Identify the blood parasite species.
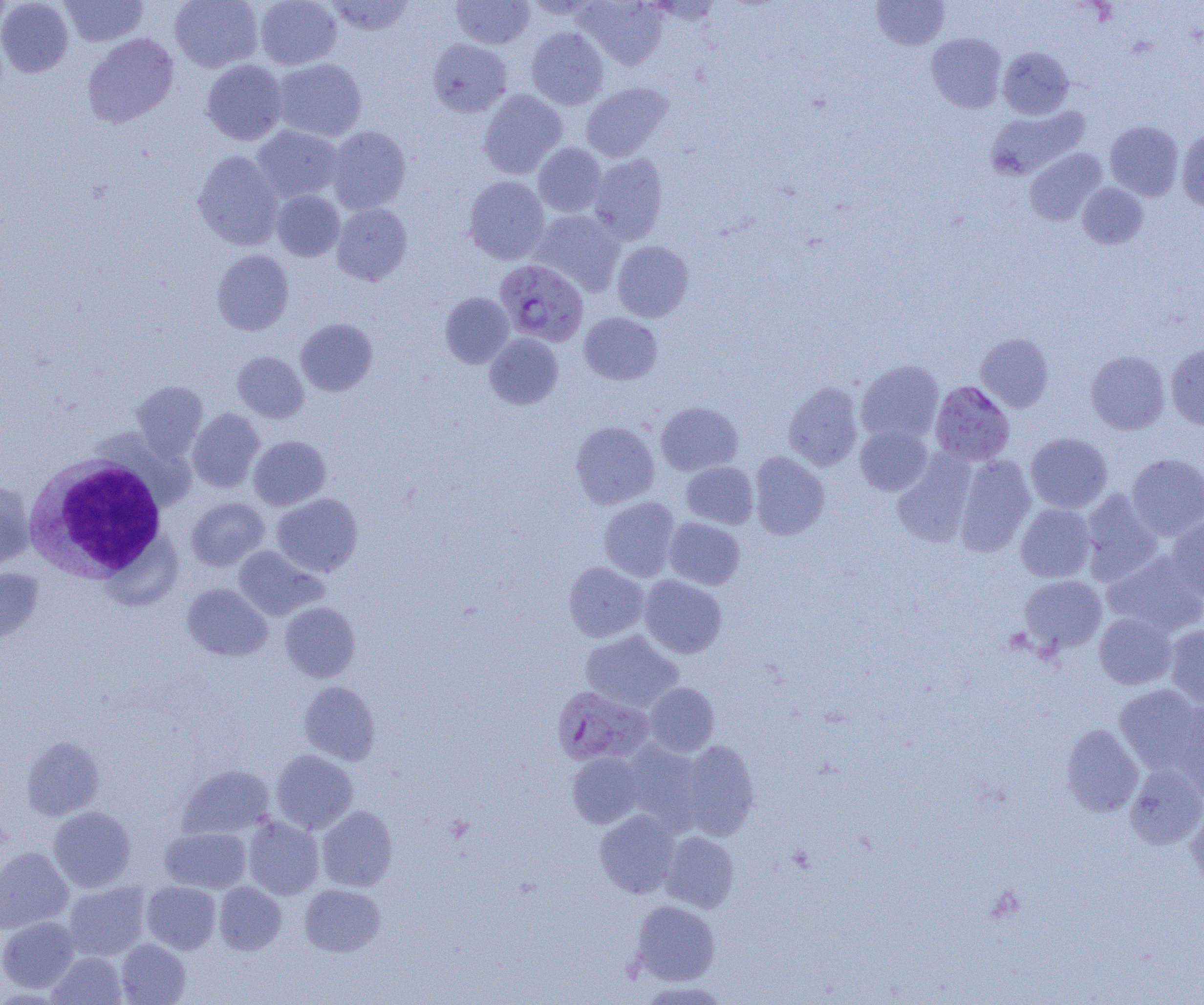
Plasmodium falciparum.

Summary:
  - Coordinate format: approximate bounding boxes as (x1, y1, x2, y2) in pixels
  - Uninfected red blood cell locations: (0, 0, 13, 32), (0, 0, 74, 77), (60, 0, 148, 46), (170, 0, 262, 72), (255, 0, 342, 70), (326, 0, 415, 37), (451, 0, 535, 49), (576, 0, 667, 70), (871, 0, 950, 50), (526, 27, 609, 109), (82, 33, 179, 128), (926, 33, 1007, 113), (427, 39, 512, 117), (998, 46, 1074, 119), (272, 58, 367, 141), (202, 60, 287, 145), (581, 82, 672, 162), (478, 89, 567, 178), (986, 105, 1089, 181), (1105, 121, 1184, 201), (252, 125, 342, 203), (326, 126, 411, 214), (1176, 129, 1204, 211), (533, 143, 606, 216), (1025, 148, 1106, 226), (193, 150, 284, 250), (588, 153, 668, 244), (464, 176, 550, 264), (1077, 183, 1148, 249), (272, 190, 344, 261), (331, 203, 412, 285), (530, 209, 625, 295), (612, 240, 694, 322), (212, 250, 294, 335), (440, 292, 514, 368), (579, 312, 662, 385), (296, 318, 377, 396), (484, 333, 563, 409), (975, 333, 1054, 412), (1166, 343, 1204, 430), (1085, 350, 1170, 435), (232, 351, 309, 423), (856, 359, 944, 443), (131, 380, 208, 460), (783, 381, 864, 471), (656, 401, 743, 476), (187, 408, 264, 492), (570, 421, 659, 509), (855, 424, 932, 495), (1025, 433, 1113, 513), (249, 436, 330, 510), (892, 451, 978, 547), (749, 452, 830, 539), (1126, 453, 1204, 540), (953, 454, 1036, 557), (681, 461, 759, 529), (0, 481, 35, 568), (1080, 489, 1163, 583), (272, 493, 363, 576), (598, 496, 680, 581), (186, 497, 269, 570), (1015, 504, 1096, 582), (1166, 516, 1204, 602), (664, 517, 745, 590), (233, 545, 325, 620), (1102, 550, 1204, 637), (563, 561, 649, 642), (0, 568, 43, 644), (639, 575, 727, 658), (1019, 575, 1107, 653), (182, 583, 272, 661), (280, 602, 360, 682), (1094, 612, 1177, 689), (1165, 624, 1204, 707), (579, 630, 684, 714), (299, 681, 381, 765), (644, 682, 719, 757), (1113, 685, 1203, 772), (1172, 702, 1204, 802), (1061, 723, 1143, 816), (23, 736, 104, 820), (677, 740, 759, 840), (621, 741, 706, 830), (271, 750, 357, 833), (566, 751, 647, 828), (1124, 762, 1204, 850), (176, 764, 275, 840), (1186, 805, 1204, 892), (49, 806, 136, 891), (317, 806, 397, 891), (595, 809, 681, 898), (243, 814, 324, 899), (159, 827, 251, 893), (660, 831, 740, 912), (0, 847, 73, 933), (64, 881, 150, 960), (141, 881, 221, 954), (214, 881, 286, 954), (300, 884, 385, 956), (631, 900, 720, 985), (0, 916, 79, 993), (116, 939, 190, 1005), (48, 951, 126, 1005), (638, 980, 731, 1004)
  - White blood cell locations: (25, 452, 168, 582)
  - Plasmodium falciparum-infected red blood cell locations: (495, 260, 589, 347), (930, 381, 1015, 466), (551, 686, 654, 766)
  - Image size: 1204×1005 pixels
  - Magnification: 1000x
  - Preparation: thin blood smear
  - Field of view: single
  - Modality: light microscopy